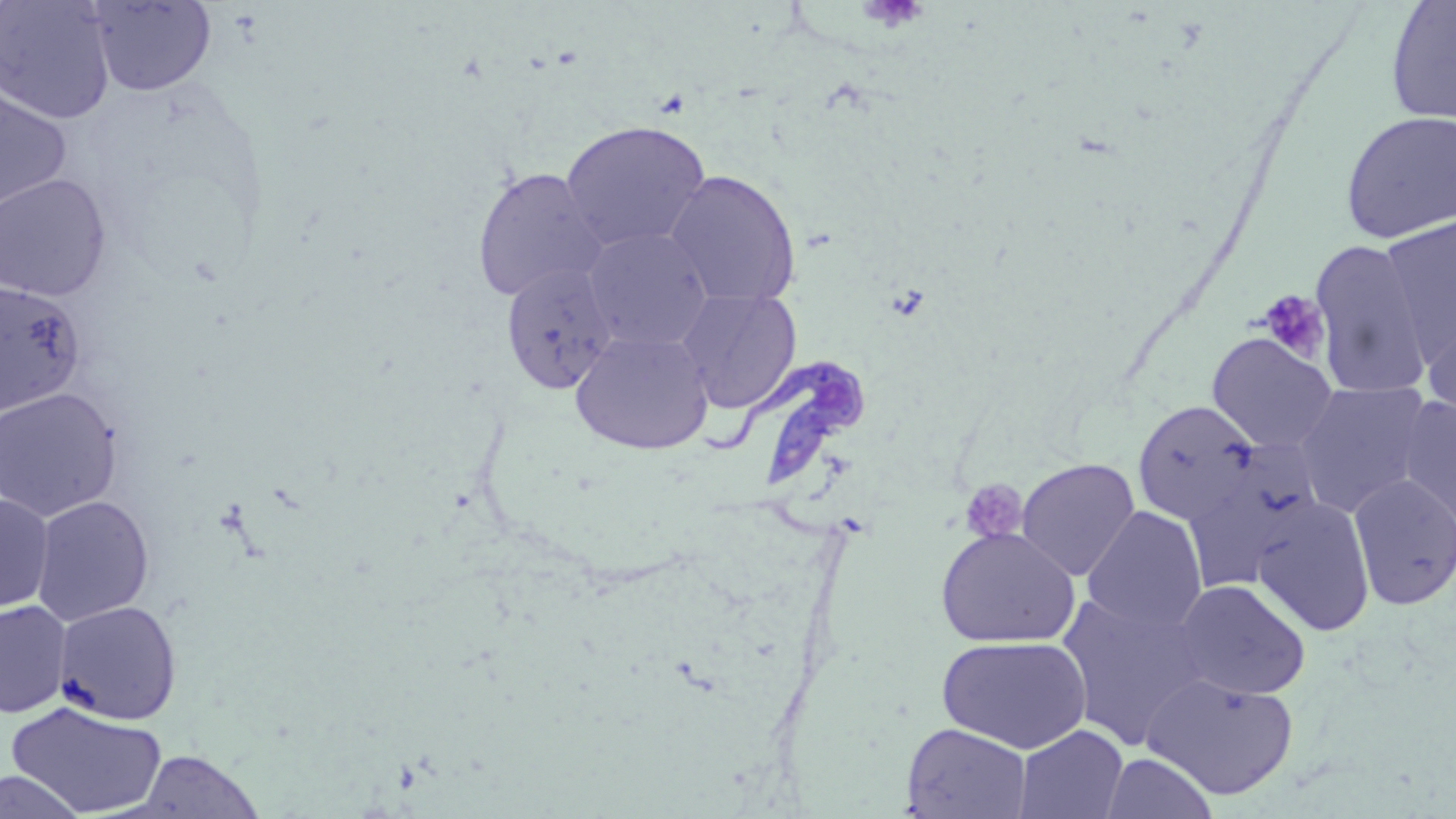

slide-level diagnosis = Trypanosoma brucei
stain = May-Grünwald-Giemsa
field of view = one of a larger specimen
modality = optical microscopy
preparation = thin blood smear
image size = 1456×819 pixels
magnification = 1000x
platelet locations = approximate bounding boxes as named x1/y1/x2/y2 corners in pixels: (x1=857, y1=1, x2=929, y2=33), (x1=1256, y1=289, x2=1331, y2=364), (x1=959, y1=478, x2=1029, y2=543)
Trypanosoma brucei locations = approximate bounding boxes as named x1/y1/x2/y2 corners in pixels: (x1=703, y1=357, x2=870, y2=488)
uninfected red blood cell locations = approximate bounding boxes as named x1/y1/x2/y2 corners in pixels: (x1=0, y1=1, x2=115, y2=124), (x1=86, y1=1, x2=217, y2=96), (x1=1384, y1=1, x2=1456, y2=126), (x1=0, y1=89, x2=71, y2=211), (x1=1339, y1=109, x2=1456, y2=245), (x1=560, y1=120, x2=711, y2=252), (x1=472, y1=166, x2=607, y2=303), (x1=665, y1=171, x2=801, y2=307), (x1=0, y1=174, x2=111, y2=301), (x1=1376, y1=216, x2=1455, y2=364), (x1=582, y1=227, x2=714, y2=352), (x1=1308, y1=238, x2=1435, y2=397), (x1=500, y1=263, x2=619, y2=395), (x1=0, y1=279, x2=85, y2=414), (x1=676, y1=288, x2=802, y2=413), (x1=1421, y1=313, x2=1455, y2=427), (x1=570, y1=330, x2=714, y2=455), (x1=1206, y1=332, x2=1340, y2=453), (x1=1293, y1=382, x2=1433, y2=515), (x1=0, y1=387, x2=123, y2=522), (x1=1395, y1=396, x2=1456, y2=531), (x1=1132, y1=399, x2=1260, y2=526), (x1=1181, y1=442, x2=1323, y2=593), (x1=1016, y1=458, x2=1140, y2=580), (x1=1348, y1=474, x2=1456, y2=611), (x1=0, y1=495, x2=54, y2=613), (x1=31, y1=495, x2=154, y2=626), (x1=1252, y1=498, x2=1375, y2=637), (x1=1081, y1=507, x2=1207, y2=633), (x1=934, y1=527, x2=1080, y2=649), (x1=1174, y1=579, x2=1311, y2=700), (x1=1056, y1=591, x2=1211, y2=750), (x1=0, y1=600, x2=72, y2=718), (x1=54, y1=600, x2=182, y2=724), (x1=936, y1=635, x2=1092, y2=754), (x1=1141, y1=672, x2=1299, y2=800), (x1=7, y1=701, x2=167, y2=817), (x1=901, y1=723, x2=1032, y2=818), (x1=1013, y1=724, x2=1129, y2=819), (x1=132, y1=749, x2=265, y2=818), (x1=1101, y1=752, x2=1218, y2=818), (x1=0, y1=769, x2=87, y2=819)